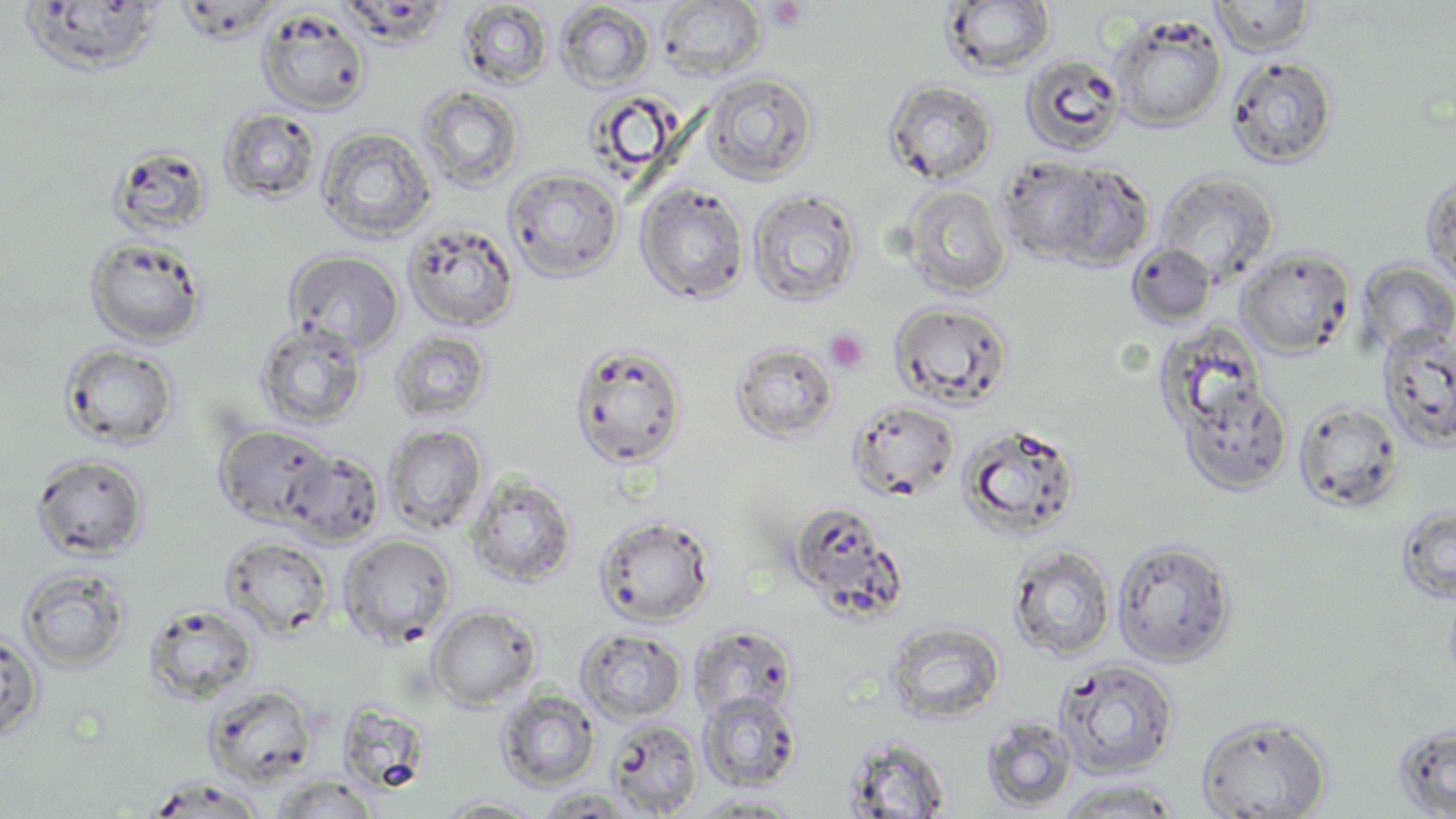

{
  "slide_level_diagnosis": "no evidence of blood parasites",
  "uninfected_red_blood_cell_locations": "approximate bounding boxes as (x1,y1)-(x2,y2) corner pairs in pixels: (1210,0)-(1316,56), (175,1)-(282,43), (655,1)-(766,80), (940,1)-(1057,78), (16,2)-(166,76), (457,2)-(553,90), (555,2)-(655,91), (255,7)-(372,116), (1108,13)-(1229,131), (1020,53)-(1126,156), (1225,55)-(1338,169), (699,72)-(819,186), (883,78)-(997,185), (417,85)-(525,192), (219,107)-(322,205), (315,125)-(437,245), (106,143)-(213,240), (998,156)-(1107,264), (1053,161)-(1155,270), (504,167)-(624,282), (1155,170)-(1280,283), (1421,170)-(1456,294), (636,181)-(749,305), (900,184)-(1013,299), (748,187)-(863,308), (403,222)-(520,332), (84,235)-(209,347), (1126,243)-(1217,326), (1237,248)-(1356,357), (283,249)-(405,356), (1355,259)-(1456,358), (889,301)-(1015,411), (254,320)-(369,430), (1377,324)-(1456,452), (389,329)-(493,424), (568,341)-(689,469), (729,341)-(840,444), (58,342)-(180,450), (1179,380)-(1293,495), (1294,398)-(1406,513), (847,400)-(961,502), (956,421)-(1082,539), (213,423)-(336,527), (382,423)-(488,535), (282,447)-(386,548), (30,453)-(149,560), (466,472)-(577,588), (787,501)-(904,615), (1395,504)-(1456,603), (593,513)-(717,627), (339,534)-(456,648), (220,535)-(334,640), (1112,538)-(1237,667), (1008,543)-(1116,661), (17,565)-(131,672), (144,602)-(260,705), (428,604)-(542,710), (883,622)-(1006,725), (688,623)-(799,721), (576,628)-(687,724), (0,629)-(44,741), (1055,659)-(1179,778), (495,689)-(601,790), (697,691)-(802,791), (604,712)-(803,808), (1196,715)-(1332,818), (981,716)-(1078,812), (605,718)-(702,817), (1393,723)-(1456,817), (842,735)-(953,817), (268,775)-(382,818), (143,777)-(268,818), (1050,778)-(1188,818), (532,787)-(647,817), (685,793)-(808,817), (433,796)-(546,818)",
  "field_of_view": "single",
  "preparation": "thin blood film",
  "image_size": "1456×819 pixels",
  "platelet_locations": "approximate bounding boxes as (x1,y1)-(x2,y2) corner pairs in pixels: (824,327)-(870,373)",
  "modality": "light microscopy",
  "magnification": "1000x",
  "stain": "May-Grünwald-Giemsa"
}